Give the position of every malaria parasite.
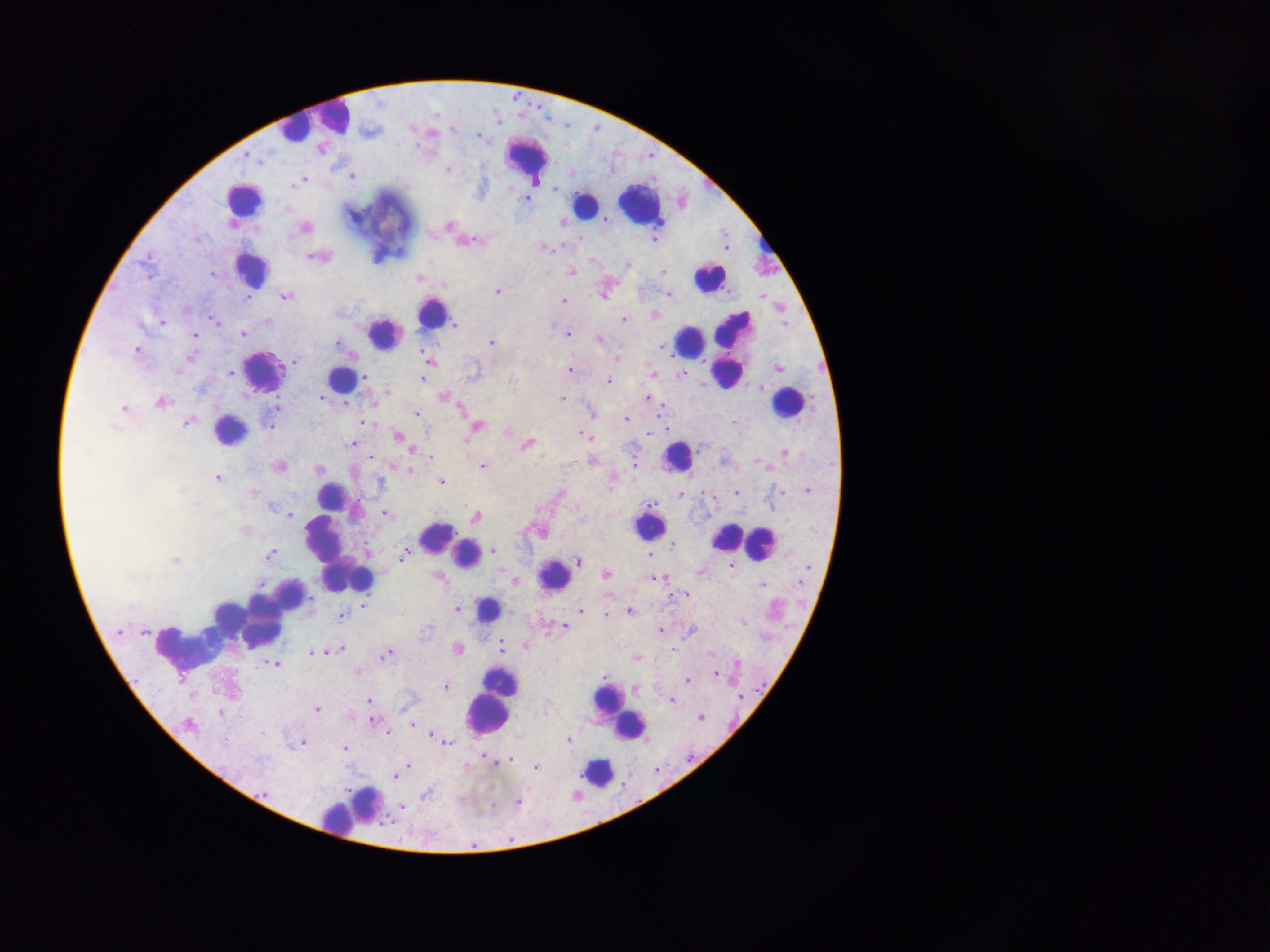

Approximate centers as x y in pixels.
Malaria parasites: 257 159; 447 170; 352 176; 302 180; 524 198; 449 225; 305 228; 654 240; 470 242; 543 247; 317 256; 627 264; 663 271; 571 272; 212 275; 419 277; 498 291; 668 293; 286 296; 248 299; 563 300; 186 309; 624 319; 214 320; 268 321; 162 322; 455 324; 243 333; 568 334; 195 335; 598 339; 491 342; 336 344; 662 347; 137 350; 190 357; 617 358; 429 360; 294 361; 778 368; 570 370; 179 371; 230 372; 653 373; 682 374; 365 376; 423 380; 608 381; 760 386; 386 393; 444 397; 322 398; 562 398; 647 398; 161 403; 346 404; 275 407; 123 408; 459 408; 417 413; 592 414; 626 420; 188 422; 365 422; 733 422; 269 424; 477 426; 114 428; 508 430; 586 436; 399 437; 352 444; 527 445; 785 453; 431 457; 591 461; 634 462; 758 462; 279 466; 482 466; 318 469; 409 470; 216 478; 441 482; 808 490; 181 491; 782 491; 560 492; 253 493; 736 493; 680 496; 274 509; 385 514; 288 515; 476 517; 245 530; 674 544; 672 548; 493 551; 404 554; 269 555; 648 555; 175 560; 579 560; 732 565; 809 568; 701 571; 606 574; 129 576; 437 576; 656 579; 515 581; 762 585; 686 594; 363 605; 457 609; 580 611; 629 611; 346 612; 606 615; 342 616; 743 621; 565 627; 661 631; 120 632; 145 633; 501 645; 340 649; 458 649; 332 650; 672 650; 313 652; 387 654; 711 654; 636 658; 737 663; 274 665; 715 674; 688 681; 446 686; 367 700; 671 700; 317 710; 220 713; 701 717; 373 721; 412 724; 187 725; 387 734; 433 735; 568 740; 303 743; 448 743; 345 748; 486 759; 511 760; 496 763; 409 767; 536 768; 395 776; 427 793; 266 794; 518 802; 402 807.

image_size: 1270×952 pixels
preparation: thick blood film
leukocyte_locations: 'approximate centers as x y in pixels: 329 118; 296 126; 528 159; 243 200; 640 202; 586 204; 766 243; 251 268; 710 276; 431 313; 384 333; 688 342; 731 350; 263 369; 338 379; 786 403; 230 430; 676 457; 329 495; 648 525; 726 536; 436 537; 759 545; 335 551; 466 554; 554 575; 361 580; 487 610; 247 621; 186 647; 607 702; 487 713; 629 725; 597 772; 356 806; 339 819'
field_of_view: single
country: Ghana
capture: mobile-phone photograph through a microscope